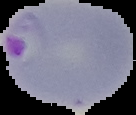 Segmented cell region on a black background. Image is 136×115 pixels. From a thin blood smear. Malaria status: parasitized.